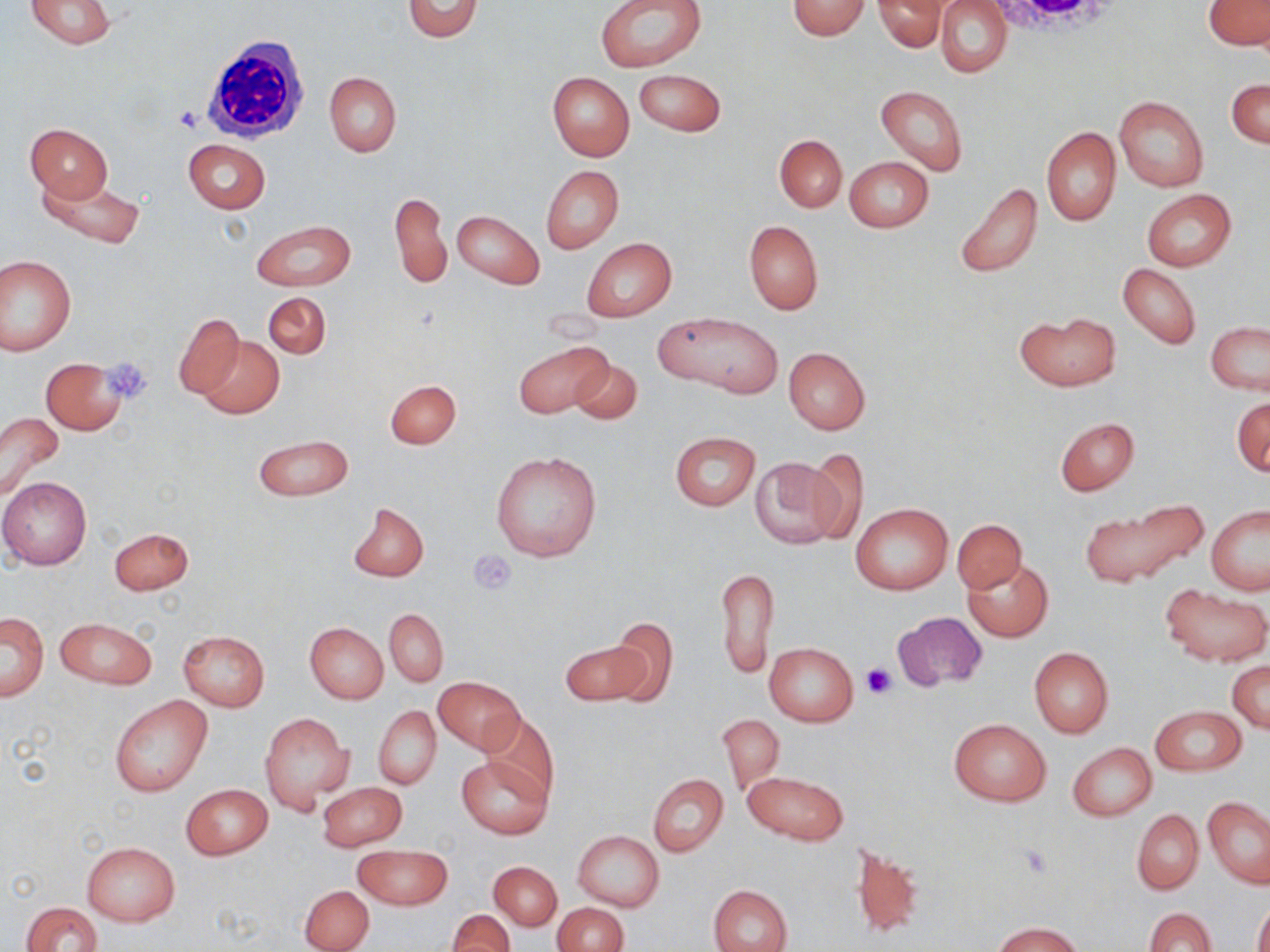

Summary:
  - Coordinate format: approximate bounding boxes as [x1, y1, x2, y2] in pixels
  - White blood cell locations: [202, 31, 314, 144]
  - Uninfected red blood cell locations: [25, 0, 118, 49], [403, 0, 483, 41], [599, 0, 704, 72], [936, 0, 1013, 77], [1204, 0, 1269, 50], [787, 1, 871, 39], [875, 1, 948, 51], [632, 69, 725, 135], [547, 72, 634, 161], [324, 73, 401, 157], [1227, 78, 1269, 148], [876, 85, 968, 176], [1114, 95, 1209, 191], [25, 123, 112, 204], [1042, 126, 1121, 226], [774, 134, 847, 212], [183, 139, 269, 213], [845, 157, 932, 232], [541, 165, 624, 254], [35, 174, 145, 249], [952, 181, 1044, 280], [1142, 189, 1235, 272], [390, 191, 451, 291], [453, 210, 544, 289], [251, 219, 356, 290], [743, 220, 823, 315], [582, 238, 676, 322], [0, 255, 76, 355], [1117, 263, 1201, 350], [264, 292, 331, 359], [1014, 311, 1120, 391], [173, 312, 245, 399], [656, 312, 782, 397], [1206, 322, 1270, 395], [196, 335, 283, 419], [513, 341, 612, 418], [783, 347, 871, 435], [41, 358, 127, 436], [567, 359, 642, 427], [385, 379, 462, 449], [1232, 397, 1270, 477], [0, 413, 65, 502], [1055, 417, 1140, 495], [669, 432, 761, 511], [253, 435, 353, 501], [802, 448, 869, 545], [490, 451, 601, 562], [750, 458, 841, 549], [0, 477, 92, 570], [1081, 500, 1210, 589], [348, 502, 429, 582], [851, 502, 952, 596], [1207, 505, 1270, 594], [953, 519, 1026, 593], [108, 526, 193, 594], [964, 559, 1053, 642], [714, 567, 778, 678], [1162, 585, 1269, 666], [384, 608, 448, 687], [893, 610, 986, 692], [1, 612, 48, 701], [55, 617, 158, 690], [605, 617, 680, 707], [305, 622, 388, 703], [178, 630, 270, 712], [560, 636, 650, 706], [764, 642, 858, 726], [1028, 647, 1114, 738], [1227, 661, 1269, 733], [434, 676, 522, 755], [109, 695, 213, 796], [373, 706, 441, 790], [1151, 706, 1245, 775], [260, 711, 355, 813], [480, 713, 559, 804], [717, 714, 784, 796], [949, 719, 1050, 805], [1069, 743, 1156, 820], [457, 755, 553, 838], [743, 770, 848, 847], [648, 774, 727, 857], [318, 782, 407, 851], [181, 784, 271, 860], [1203, 796, 1270, 888], [1132, 809, 1203, 894], [574, 831, 664, 911], [82, 841, 179, 926], [352, 842, 453, 910], [848, 843, 922, 939], [489, 861, 562, 929], [707, 884, 792, 952], [301, 885, 374, 952], [1253, 899, 1270, 952], [20, 901, 102, 952], [553, 903, 630, 952], [1144, 907, 1214, 952], [447, 909, 515, 951], [994, 920, 1081, 952]
  - Platelet locations: [175, 107, 204, 131], [104, 357, 152, 401], [470, 548, 516, 593], [862, 663, 893, 698], [1019, 843, 1056, 879]
  - Slide-level diagnosis: no evidence of blood parasites
  - Magnification: 1000x
  - Modality: optical microscopy
  - Field of view: one of a larger specimen
  - Image size: 1270×952 pixels
  - Preparation: thin blood smear
  - Stain: May-Grünwald-Giemsa